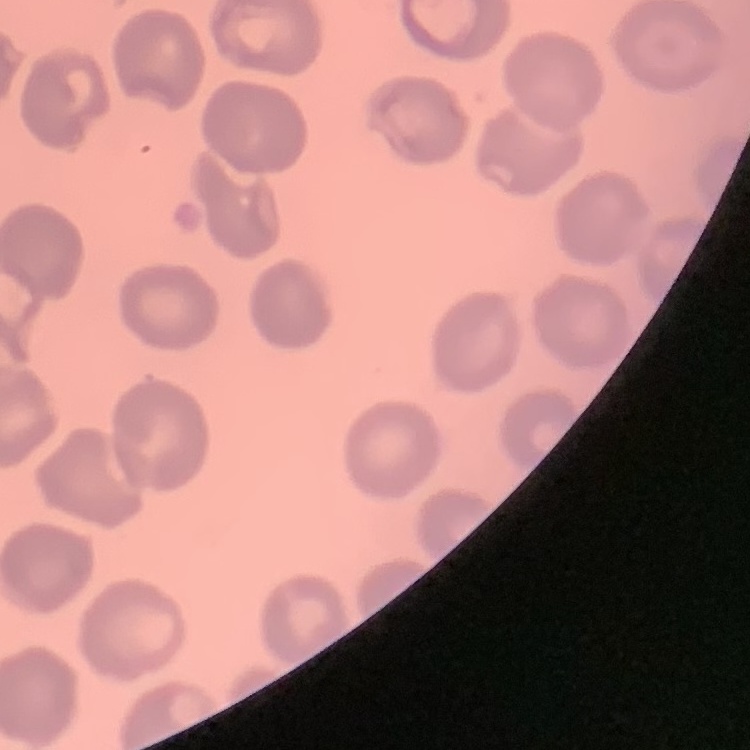

{
  "red_blood_cell_morphology": "no rouleaux formation",
  "image_type": "one tile cut from a larger photomicrograph",
  "preparation": "thin blood smear",
  "stain": "Field's or Giemsa"
}